Name the blood parasite species.
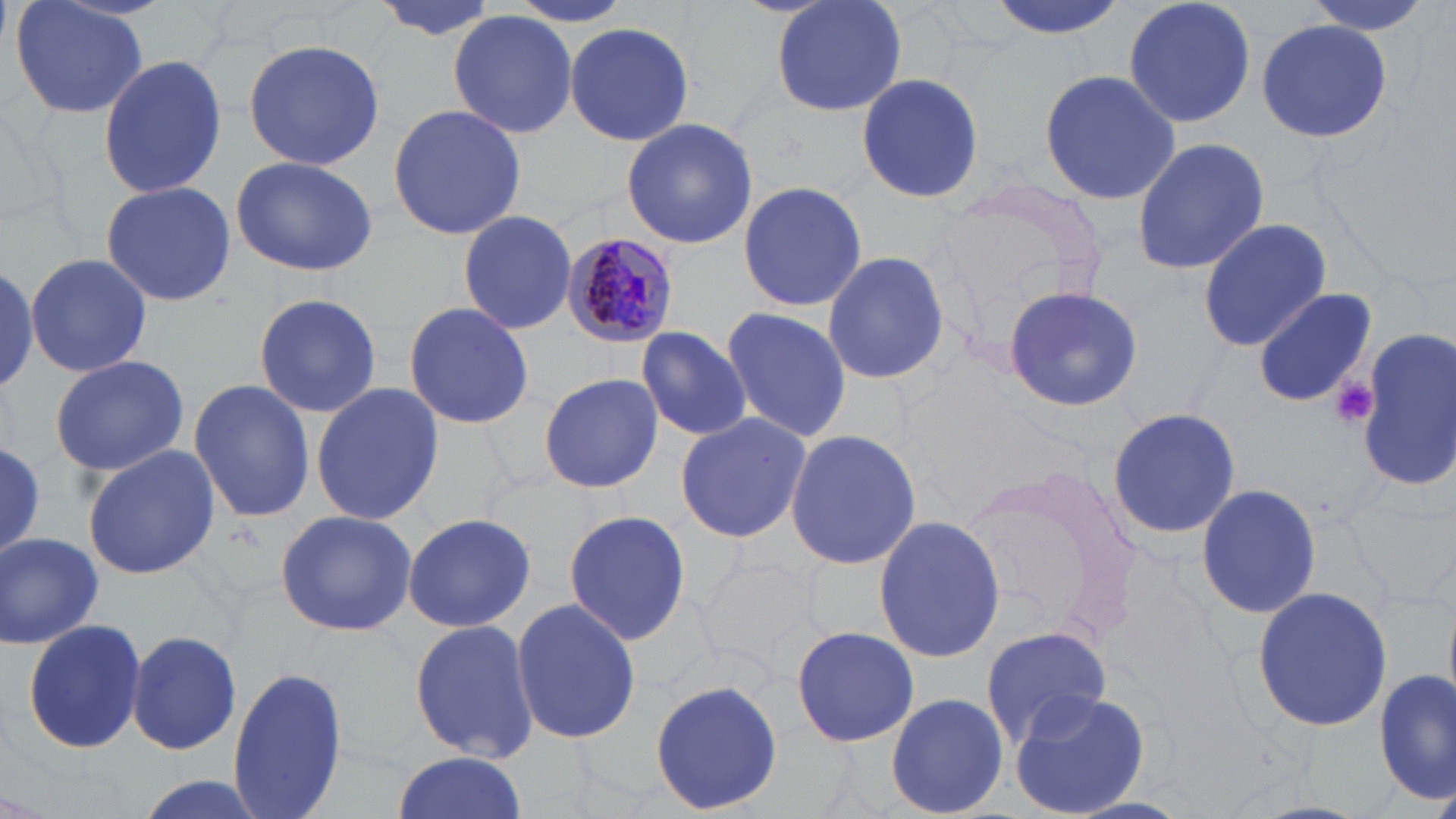

Plasmodium malariae.

Approximate bounding boxes as named x1/y1/x2/y2 corners in pixels. Platelet locations: (x1=1329, y1=376, x2=1378, y2=430). Plasmodium malariae-infected red blood cell locations: (x1=561, y1=233, x2=678, y2=348). Uninfected red blood cell locations: (x1=10, y1=0, x2=150, y2=121), (x1=369, y1=0, x2=502, y2=40), (x1=769, y1=0, x2=909, y2=120), (x1=982, y1=0, x2=1131, y2=38), (x1=1123, y1=0, x2=1260, y2=128), (x1=1304, y1=0, x2=1435, y2=37), (x1=448, y1=11, x2=579, y2=139), (x1=1254, y1=18, x2=1392, y2=141), (x1=563, y1=21, x2=694, y2=146), (x1=586, y1=23, x2=722, y2=225), (x1=243, y1=39, x2=385, y2=172), (x1=99, y1=55, x2=229, y2=197), (x1=1038, y1=67, x2=1179, y2=206), (x1=854, y1=71, x2=987, y2=205), (x1=388, y1=103, x2=525, y2=240), (x1=620, y1=117, x2=757, y2=250), (x1=1131, y1=135, x2=1270, y2=275), (x1=230, y1=156, x2=378, y2=277), (x1=99, y1=180, x2=235, y2=307), (x1=737, y1=180, x2=867, y2=313), (x1=924, y1=184, x2=1111, y2=353), (x1=457, y1=210, x2=578, y2=336), (x1=1197, y1=218, x2=1331, y2=353), (x1=821, y1=249, x2=950, y2=387), (x1=25, y1=250, x2=152, y2=379), (x1=0, y1=259, x2=42, y2=393), (x1=1002, y1=284, x2=1142, y2=415), (x1=1251, y1=286, x2=1376, y2=406), (x1=253, y1=293, x2=382, y2=419), (x1=403, y1=302, x2=534, y2=430), (x1=720, y1=306, x2=849, y2=444), (x1=633, y1=326, x2=752, y2=442), (x1=1355, y1=329, x2=1454, y2=490), (x1=49, y1=353, x2=190, y2=477), (x1=540, y1=372, x2=665, y2=494), (x1=188, y1=379, x2=315, y2=525), (x1=310, y1=381, x2=443, y2=528), (x1=1106, y1=406, x2=1244, y2=542), (x1=674, y1=413, x2=811, y2=543), (x1=783, y1=429, x2=921, y2=571), (x1=0, y1=436, x2=45, y2=563), (x1=81, y1=446, x2=221, y2=581), (x1=962, y1=460, x2=1146, y2=647), (x1=1195, y1=482, x2=1322, y2=618), (x1=1347, y1=484, x2=1456, y2=602), (x1=562, y1=510, x2=691, y2=647), (x1=274, y1=511, x2=416, y2=637), (x1=401, y1=511, x2=539, y2=632), (x1=872, y1=516, x2=1006, y2=662), (x1=2, y1=532, x2=103, y2=648), (x1=698, y1=550, x2=822, y2=674), (x1=1250, y1=586, x2=1394, y2=731), (x1=511, y1=596, x2=641, y2=746), (x1=20, y1=617, x2=148, y2=757), (x1=409, y1=618, x2=540, y2=764), (x1=980, y1=624, x2=1112, y2=748), (x1=790, y1=625, x2=919, y2=748), (x1=125, y1=630, x2=244, y2=756), (x1=225, y1=665, x2=351, y2=819), (x1=1376, y1=668, x2=1454, y2=802), (x1=649, y1=679, x2=783, y2=813), (x1=1007, y1=688, x2=1154, y2=817), (x1=885, y1=691, x2=1009, y2=818), (x1=389, y1=752, x2=528, y2=819), (x1=125, y1=776, x2=272, y2=819). One field of a larger specimen. Image is 1456×819 pixels. Light microscopy. 1000x magnification. May-Grünwald-Giemsa-stained preparation. Thin blood smear.